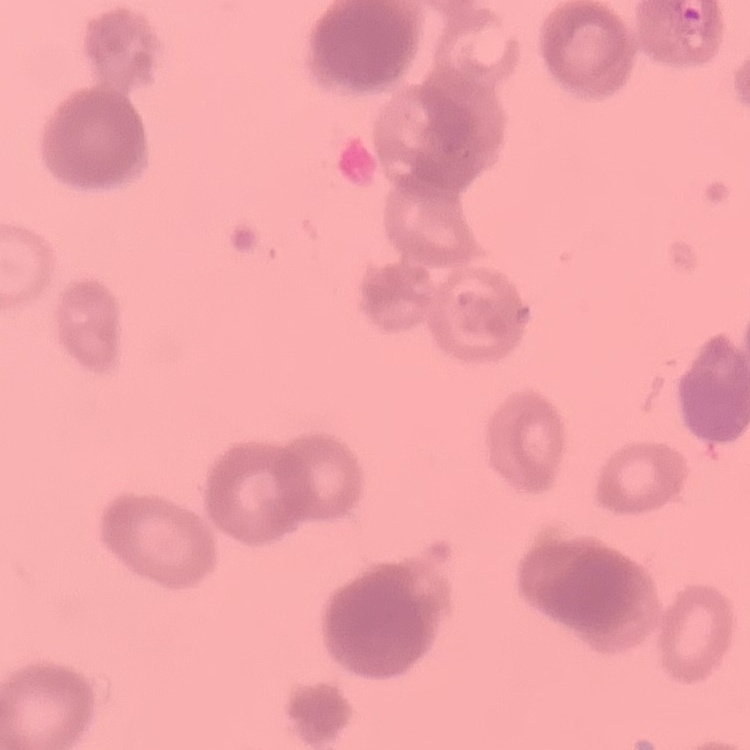
{
  "red_blood_cell_morphology": "rouleaux formation",
  "preparation": "thin blood smear",
  "stain": "Field's or Giemsa",
  "image_type": "one tile cut from a larger photomicrograph"
}